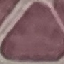

malaria_status: uninfected
image_type: cell patch, automatically extracted from a larger field of view and resized to 64 × 64 pixels
stain: Giemsa
preparation: thin blood smear
capture: smartphone through the microscope eyepiece